Name the cell type shown.
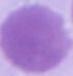
An erythrocyte.

{
  "magnification": "1000x",
  "modality": "micrograph"
}